Describe the morphology of the erythrocytes.
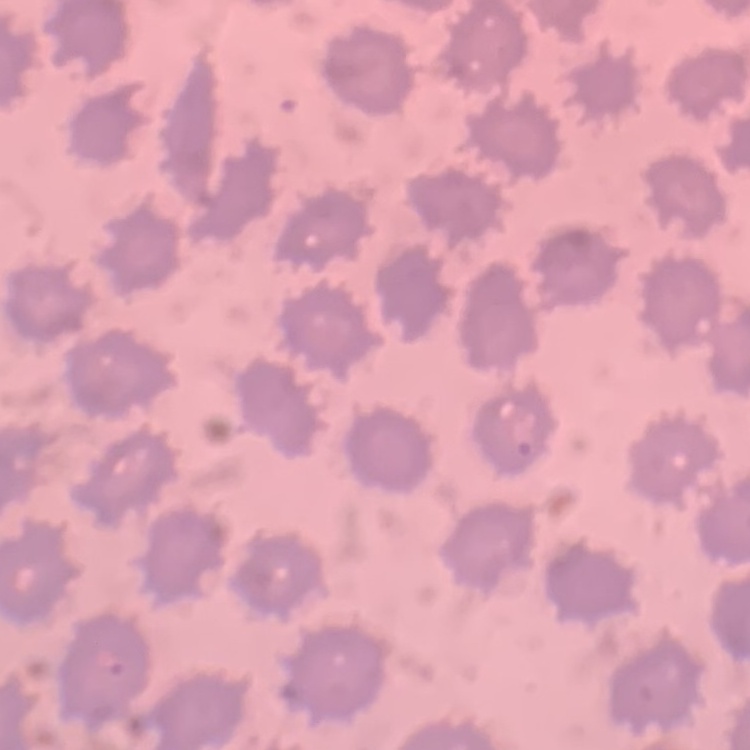

No rouleaux formation.

Summary:
  - Stain: Field's or Giemsa
  - Preparation: thin blood smear
  - Image type: square crop of a larger photomicrograph